Assess this cell for malaria.
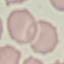
Uninfected.

Cell patch, automatically extracted from a larger field of view and resized to 64 × 64 pixels. Giemsa stain. Photographed with a smartphone camera at the microscope eyepiece. Thin blood smear.